Point out each Plasmodium parasite.
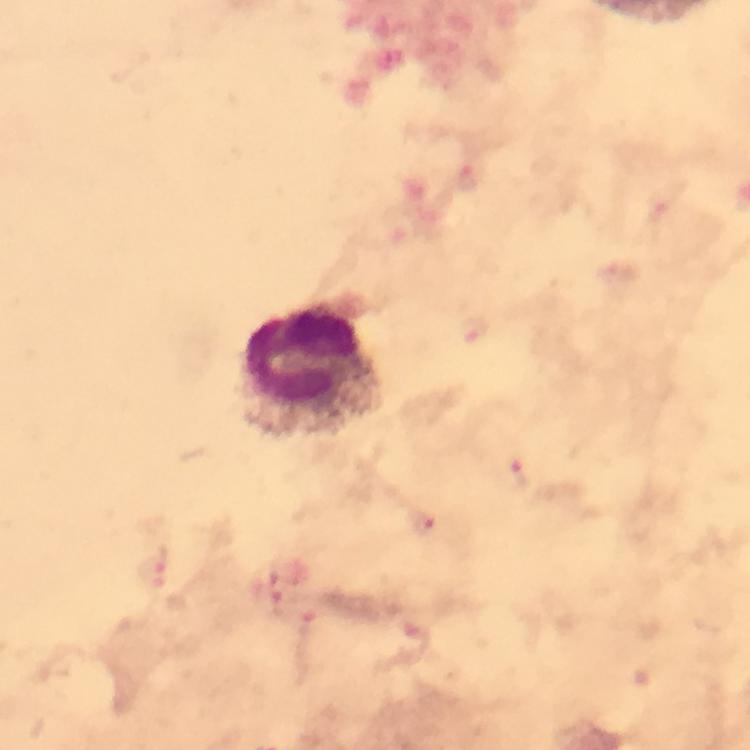

Approximate centers as (x, y) in pixels.
Plasmodium parasites: (475, 329), (515, 474), (421, 523), (150, 570), (279, 606).

Leukocyte locations: (314, 373). Immersion oil was used. Photographed with a smartphone mounted on the microscope. A crop from one field of view. Image is 750×750 pixels. At 100x magnification. Thick smear. From a malaria diagnostic workup. Giemsa stain.